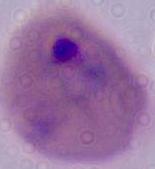
magnification = 400x or 1000x
modality = photomicrograph
identification = Plasmodium